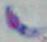

Photomicrograph. Toxoplasma gondii is seen. Captured at 1000x magnification.